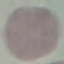
Result: no malaria parasites detected. Thin smear of blood. Automatically extracted cell patch, resized to 64 × 64 pixels. Acquired by smartphone through the microscope eyepiece. Giemsa-stained preparation.